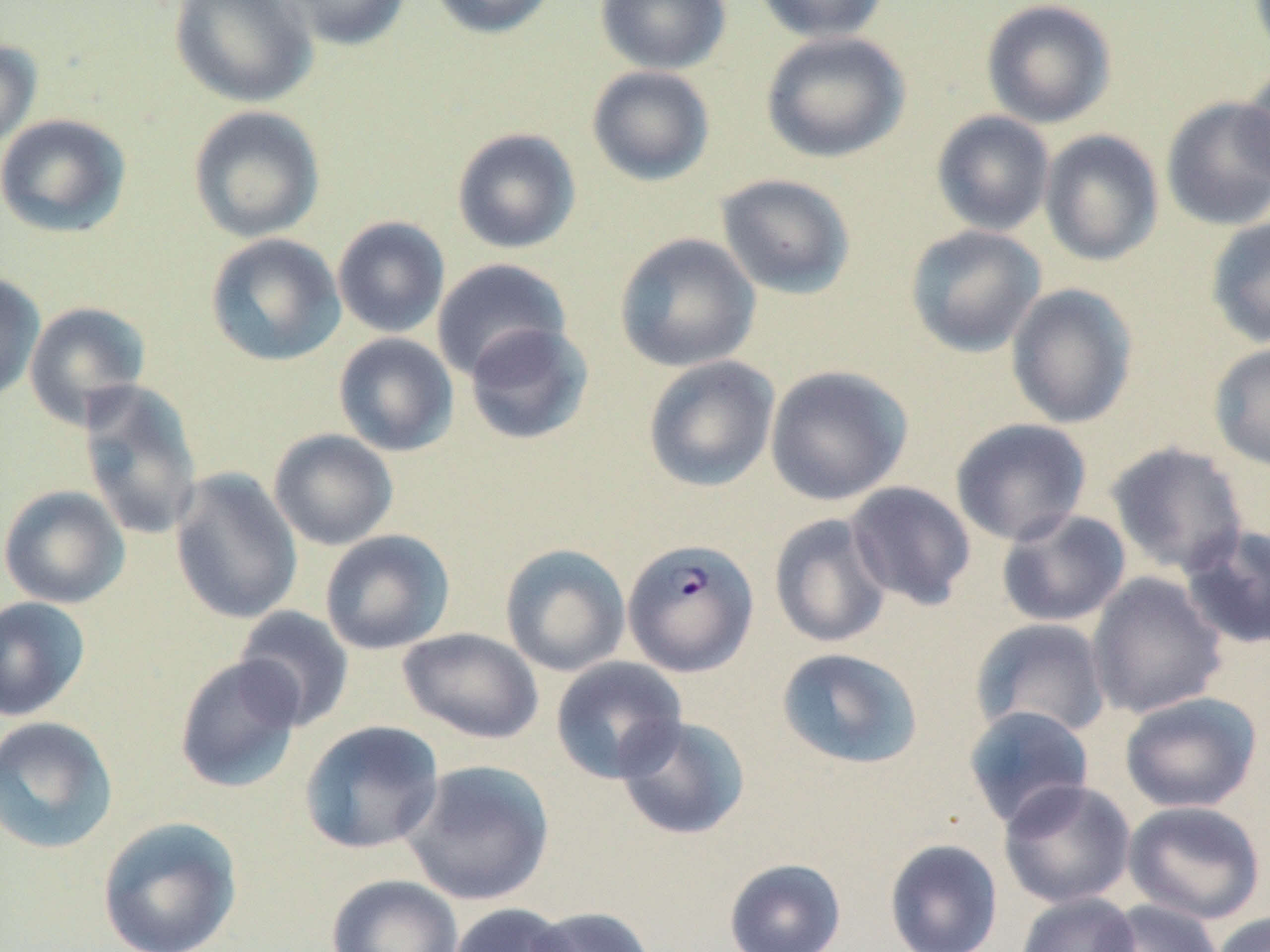
slide-level diagnosis = Plasmodium falciparum
uninfected red blood cell locations = approximate bounding boxes as [x1, y1, x2, y2] in pixels: [168, 0, 319, 108], [273, 0, 412, 50], [428, 0, 558, 39], [594, 0, 732, 75], [753, 0, 890, 43], [981, 1, 1117, 128], [760, 31, 910, 164], [0, 39, 43, 152], [1239, 61, 1270, 192], [586, 65, 715, 186], [1160, 96, 1270, 231], [187, 105, 326, 243], [931, 111, 1055, 236], [0, 113, 132, 238], [451, 127, 582, 254], [1039, 129, 1164, 266], [715, 173, 857, 300], [332, 216, 451, 338], [1204, 218, 1270, 349], [904, 224, 1047, 357], [614, 232, 761, 373], [205, 233, 346, 367], [431, 258, 572, 381], [0, 271, 46, 404], [1005, 283, 1139, 429], [24, 301, 152, 428], [463, 322, 595, 446], [333, 332, 459, 456], [1208, 341, 1270, 473], [642, 355, 780, 493], [765, 365, 913, 506], [76, 379, 204, 543], [950, 418, 1092, 546], [268, 429, 399, 550], [1105, 441, 1249, 577], [169, 467, 303, 625], [844, 481, 977, 611], [0, 484, 131, 609], [996, 508, 1131, 628], [768, 513, 893, 649], [1179, 523, 1270, 650], [319, 529, 454, 655], [499, 543, 631, 676], [1086, 572, 1227, 719], [0, 595, 91, 722], [232, 606, 355, 731], [970, 618, 1112, 740], [397, 627, 544, 744], [775, 647, 924, 770], [173, 655, 305, 794], [550, 656, 688, 784], [1119, 692, 1263, 813], [962, 704, 1095, 830], [615, 714, 751, 841], [0, 715, 119, 855], [298, 720, 444, 855], [401, 758, 555, 907], [998, 779, 1136, 909], [1123, 800, 1267, 925], [97, 816, 243, 952], [883, 838, 1004, 952], [724, 858, 847, 952], [326, 873, 464, 952], [1015, 892, 1140, 952], [1096, 899, 1224, 952], [446, 903, 578, 952], [525, 905, 656, 952], [1211, 912, 1270, 952]
field of view = single
preparation = thin blood film
stain = May-Grünwald-Giemsa
Plasmodium falciparum-infected red blood cell locations = approximate bounding boxes as [x1, y1, x2, y2] in pixels: [622, 538, 760, 677]
magnification = 1000x
modality = optical microscopy
image size = 1270×952 pixels